Identify the parasite.
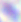
This is Toxoplasma gondii.

Micrograph. 400x magnification.